Describe the morphology of the red blood cells.
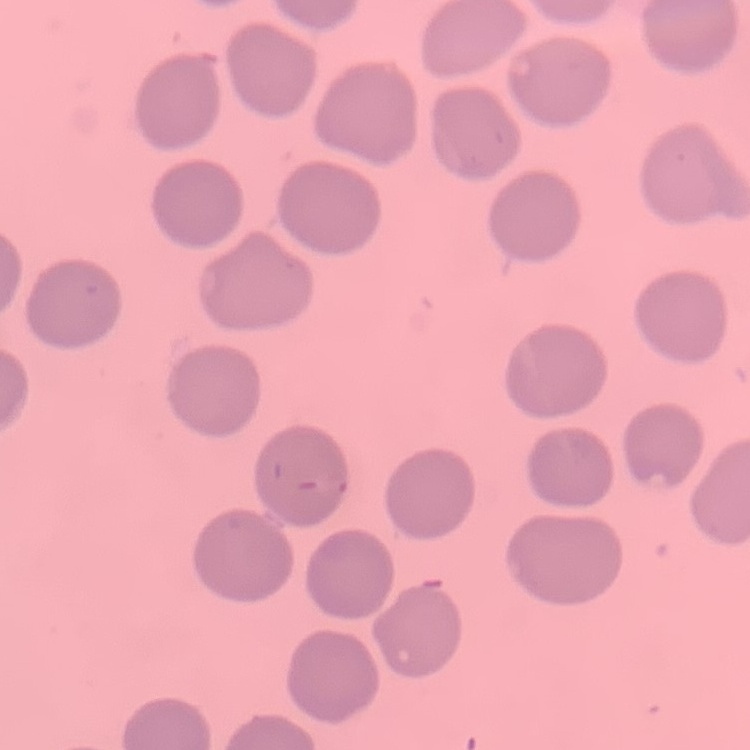
No rouleaux formation.

Summary:
  - Stain: Field's or Giemsa
  - Image type: one tile cut from a larger photomicrograph
  - Preparation: thin blood film